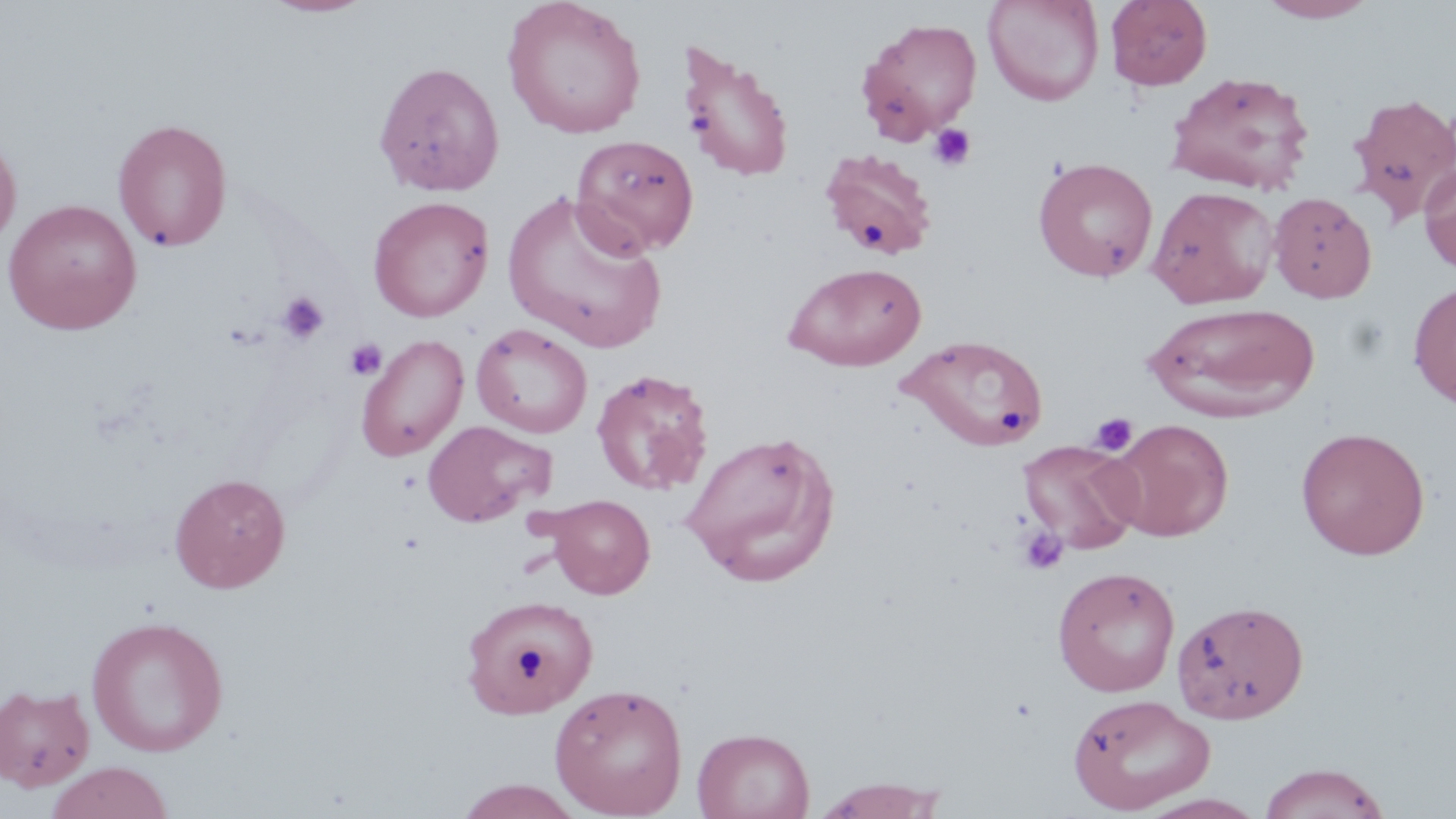

Approximate bounding boxes as (x1, y1, x2, y2) in pixels. Platelet locations: (685, 110, 716, 136), (927, 123, 976, 171), (277, 291, 328, 344), (344, 338, 387, 381), (1089, 412, 1137, 456), (1016, 525, 1068, 575). Uninfected red blood cell locations: (502, 0, 648, 140), (982, 0, 1105, 106), (1105, 0, 1213, 91), (1257, 0, 1378, 23), (259, 1, 374, 18), (857, 17, 982, 142), (678, 43, 795, 183), (373, 61, 505, 197), (1166, 70, 1316, 195), (1347, 92, 1456, 223), (112, 118, 232, 252), (0, 127, 22, 253), (571, 134, 699, 257), (817, 147, 939, 260), (1033, 157, 1159, 283), (1419, 159, 1456, 277), (1147, 185, 1280, 308), (503, 189, 668, 353), (1268, 191, 1377, 303), (368, 196, 494, 322), (2, 199, 142, 335), (784, 262, 927, 371), (1408, 281, 1456, 409), (1144, 301, 1320, 422), (472, 323, 593, 437), (897, 333, 1051, 452), (355, 334, 469, 462), (591, 367, 715, 495), (422, 419, 555, 528), (1107, 419, 1234, 541), (1295, 426, 1430, 560), (680, 429, 840, 587), (1018, 439, 1142, 554), (169, 473, 291, 593), (541, 494, 657, 599), (1052, 566, 1180, 697), (459, 592, 600, 716), (1172, 599, 1309, 724), (86, 615, 229, 758), (0, 682, 96, 792), (549, 682, 688, 818), (1067, 692, 1216, 814), (692, 727, 814, 819), (45, 761, 173, 819), (1258, 762, 1391, 819), (810, 778, 951, 818), (454, 779, 586, 818). Slide-level diagnosis: negative for blood parasites. Light microscopy. Captured at 1000x magnification. Image is 1456×819 pixels. Thin blood film. May-Grünwald-Giemsa-stained preparation. One field of a larger specimen.